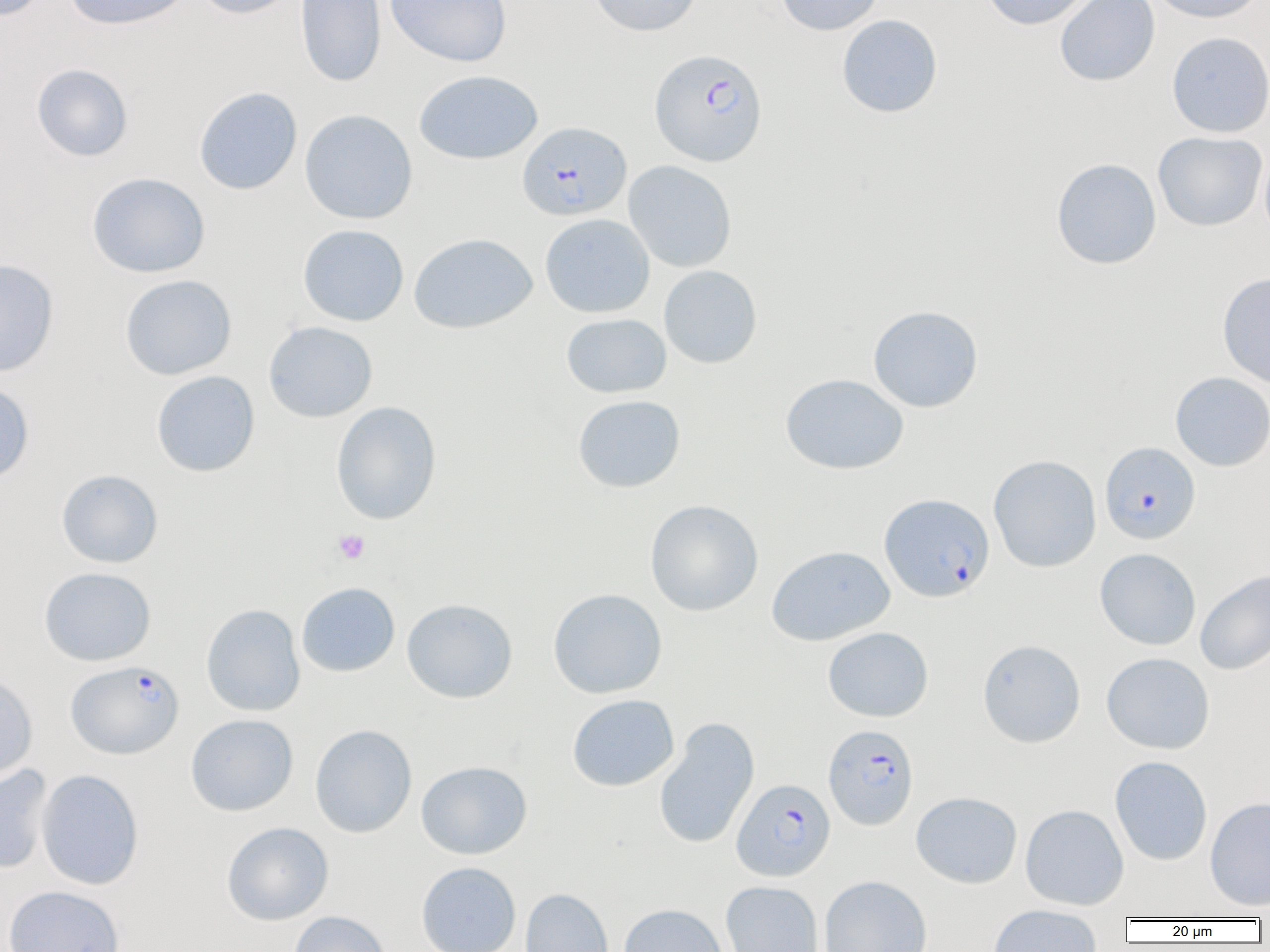

Summary:
  - Coordinate format: approximate bounding boxes as (x1, y1, x2, y2) in pixels
  - Platelet locations: (333, 529, 370, 565)
  - Uninfected red blood cell locations: (1, 0, 49, 21), (64, 0, 192, 30), (194, 0, 298, 20), (295, 0, 386, 88), (385, 0, 513, 67), (587, 0, 703, 37), (774, 0, 885, 36), (980, 0, 1095, 30), (1147, 0, 1267, 24), (1054, 1, 1160, 86), (836, 14, 943, 118), (1166, 31, 1270, 138), (31, 63, 134, 162), (414, 70, 543, 164), (194, 87, 302, 195), (299, 109, 418, 224), (1153, 131, 1267, 232), (1259, 145, 1270, 248), (1051, 158, 1162, 269), (623, 160, 737, 273), (87, 172, 210, 278), (540, 214, 655, 318), (297, 224, 409, 326), (409, 232, 537, 334), (0, 259, 59, 377), (658, 265, 762, 369), (1217, 272, 1270, 388), (120, 274, 237, 380), (867, 305, 984, 413), (561, 313, 672, 398), (263, 321, 378, 423), (151, 370, 260, 477), (1170, 372, 1270, 471), (780, 373, 909, 475), (0, 380, 35, 485), (573, 395, 686, 492), (331, 400, 442, 525), (988, 454, 1102, 573), (56, 469, 163, 568), (645, 499, 764, 616), (767, 545, 895, 646), (1095, 548, 1201, 650), (39, 567, 156, 666), (1195, 569, 1270, 676), (296, 582, 400, 677), (547, 588, 668, 699), (402, 598, 518, 703), (201, 604, 305, 717), (822, 627, 934, 722), (977, 639, 1086, 748), (1101, 652, 1215, 755), (0, 673, 38, 782), (567, 694, 679, 792), (185, 714, 298, 816), (654, 717, 760, 850), (310, 724, 417, 838), (1109, 755, 1213, 865), (416, 760, 532, 860), (0, 765, 53, 874), (36, 769, 145, 890), (911, 791, 1022, 888), (1204, 796, 1270, 911), (1020, 804, 1129, 910), (222, 822, 334, 925), (416, 862, 521, 952), (819, 875, 932, 952), (720, 881, 824, 952), (3, 885, 126, 952), (520, 888, 614, 952), (618, 903, 728, 952), (988, 905, 1103, 952), (288, 911, 392, 952)
  - Plasmodium falciparum-infected red blood cell locations: (650, 48, 768, 166), (518, 121, 632, 221), (1100, 442, 1200, 544), (879, 493, 995, 603), (65, 661, 184, 759), (823, 724, 919, 830), (732, 778, 835, 881)
  - Slide-level diagnosis: Plasmodium falciparum
  - Field of view: one of a larger specimen
  - Magnification: 1000x
  - Modality: optical microscopy
  - Image size: 1270×952 pixels
  - Preparation: thin blood smear